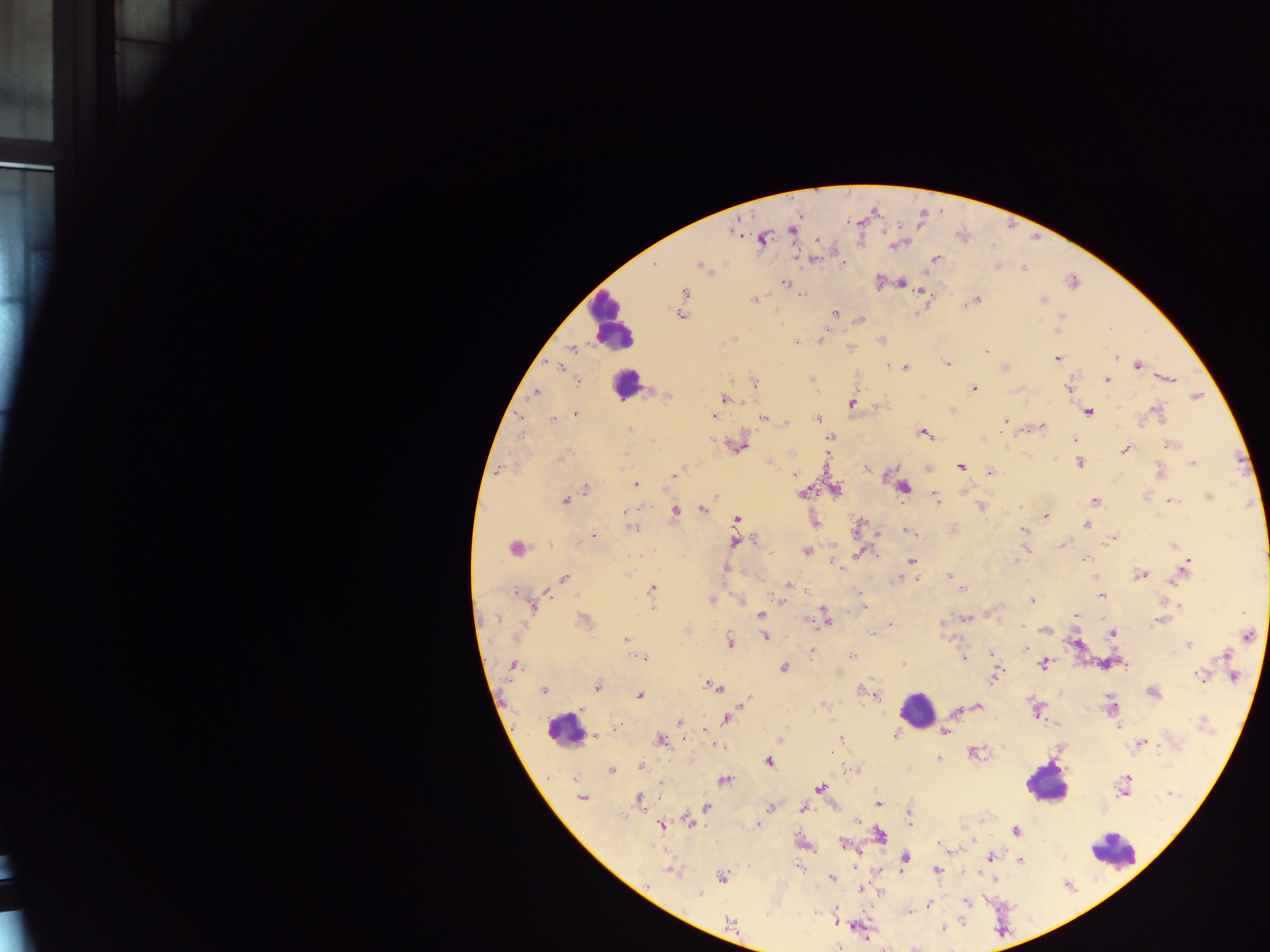

preparation = thick blood film
field of view = single
country = Ghana
Plasmodium parasite locations = approximate centers as {x, y} in pixels: {792, 229}, {733, 232}, {763, 239}, {817, 240}, {815, 258}, {934, 259}, {843, 265}, {702, 266}, {997, 266}, {1024, 268}, {1073, 282}, {784, 283}, {901, 283}, {684, 292}, {801, 294}, {976, 299}, {754, 300}, {1042, 300}, {836, 314}, {680, 315}, {1061, 316}, {861, 319}, {820, 340}, {881, 340}, {797, 342}, {573, 349}, {986, 351}, {1057, 358}, {1116, 358}, {948, 364}, {1137, 365}, {559, 367}, {905, 368}, {1170, 378}, {1106, 380}, {579, 382}, {754, 384}, {1069, 388}, {973, 389}, {535, 392}, {667, 396}, {1196, 396}, {725, 399}, {851, 404}, {1088, 411}, {1156, 412}, {576, 414}, {714, 417}, {521, 418}, {763, 418}, {818, 418}, {553, 419}, {786, 422}, {1005, 422}, {1043, 427}, {629, 430}, {924, 433}, {521, 435}, {830, 437}, {1074, 440}, {1169, 445}, {738, 447}, {1125, 449}, {561, 458}, {1079, 463}, {1193, 463}, {960, 467}, {866, 468}, {990, 472}, {1160, 472}, {794, 475}, {674, 476}, {636, 484}, {903, 487}, {586, 488}, {836, 490}, {802, 493}, {1209, 497}, {937, 499}, {565, 500}, {1095, 501}, {1171, 501}, {981, 507}, {701, 510}, {626, 511}, {674, 511}, {1046, 516}, {737, 519}, {1087, 525}, {633, 529}, {1023, 530}, {907, 531}, {593, 537}, {1113, 537}, {754, 540}, {735, 542}, {1061, 545}, {1172, 546}, {514, 548}, {1026, 549}, {805, 551}, {859, 553}, {1085, 558}, {911, 561}, {1017, 561}, {835, 563}, {1186, 564}, {726, 568}, {949, 575}, {1140, 575}, {564, 578}, {899, 578}, {788, 585}, {962, 588}, {651, 589}, {515, 591}, {547, 592}, {860, 593}, {1101, 595}, {781, 600}, {1033, 600}, {711, 601}, {742, 601}, {1179, 606}, {533, 607}, {863, 607}, {761, 615}, {1075, 616}, {965, 618}, {497, 619}, {585, 620}, {826, 620}, {806, 621}, {1159, 621}, {891, 624}, {1021, 626}, {1045, 630}, {872, 633}, {1113, 634}, {1248, 636}, {766, 637}, {625, 639}, {731, 642}, {1189, 645}, {1026, 650}, {811, 652}, {991, 654}, {1225, 655}, {853, 656}, {645, 658}, {963, 658}, {1043, 664}, {512, 665}, {903, 665}, {1125, 665}, {783, 667}, {1199, 675}, {994, 676}, {1233, 676}, {597, 686}, {713, 686}, {862, 689}, {543, 690}, {1153, 693}, {640, 696}, {877, 697}, {744, 702}, {823, 705}, {1111, 705}, {977, 706}, {583, 709}, {1036, 711}, {955, 712}, {725, 719}, {680, 722}, {1203, 723}, {1119, 727}, {618, 728}, {944, 732}, {895, 733}, {595, 736}, {841, 738}, {660, 740}, {780, 741}, {1142, 743}, {722, 747}, {973, 752}, {939, 759}, {769, 762}, {641, 767}, {854, 769}, {612, 770}, {573, 779}, {724, 780}, {661, 783}, {1125, 786}, {820, 787}, {1169, 794}, {582, 798}, {639, 798}, {878, 803}, {706, 807}, {770, 809}, {803, 809}, {910, 816}, {858, 820}, {689, 821}, {758, 824}, {660, 826}, {1015, 831}, {880, 834}, {844, 844}, {942, 845}, {991, 857}, {905, 859}, {1020, 861}, {798, 868}, {937, 870}, {672, 872}, {722, 877}, {832, 878}, {994, 879}, {861, 889}, {700, 895}, {966, 902}, {928, 906}, {909, 911}, {729, 921}, {943, 928}, {838, 947}
capture = mobile-phone photograph through a microscope
leukocyte locations = approximate centers as {x, y} in pixels: {611, 323}, {626, 385}, {916, 711}, {564, 730}, {1046, 784}, {1113, 852}
image size = 1270×952 pixels